Name the cell type shown.
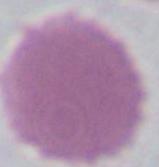

An erythrocyte.

Photomicrograph. 1000x magnification.